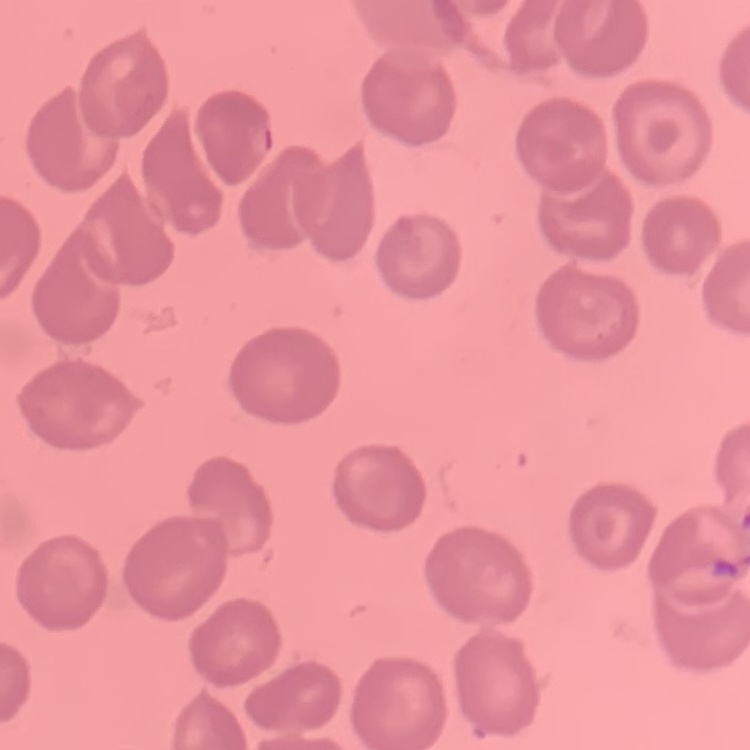
Summary:
  - Erythrocyte morphology: no rouleaux formation
  - Image type: one tile cut from a larger photomicrograph
  - Preparation: thin blood smear
  - Stain: Field's or Giemsa